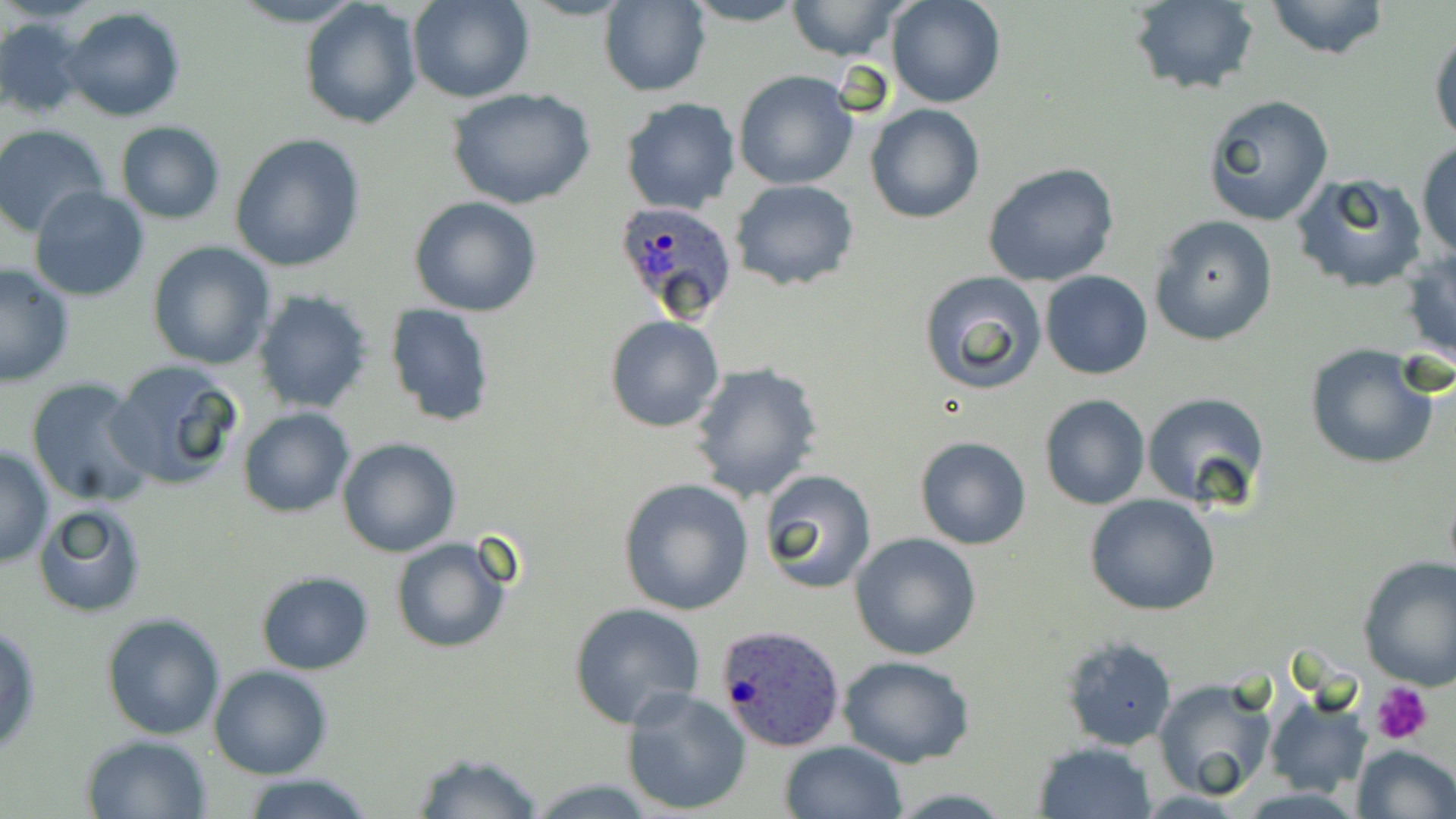
slide_level_diagnosis: Plasmodium ovale
field_of_view: one of a larger specimen
preparation: thin blood film
uninfected_red_blood_cell_locations: 'approximate bounding boxes as named x1/y1/x2/y2 corners in pixels: (x1=408, y1=0, x2=531, y2=104), (x1=599, y1=0, x2=710, y2=97), (x1=680, y1=0, x2=809, y2=27), (x1=786, y1=0, x2=909, y2=63), (x1=885, y1=0, x2=1005, y2=109), (x1=1262, y1=0, x2=1393, y2=60), (x1=298, y1=1, x2=421, y2=129), (x1=1126, y1=1, x2=1260, y2=95), (x1=61, y1=6, x2=188, y2=122), (x1=0, y1=18, x2=86, y2=118), (x1=1428, y1=20, x2=1456, y2=149), (x1=733, y1=71, x2=859, y2=190), (x1=450, y1=90, x2=595, y2=210), (x1=1204, y1=95, x2=1334, y2=225), (x1=620, y1=98, x2=742, y2=216), (x1=865, y1=102, x2=984, y2=223), (x1=115, y1=121, x2=226, y2=224), (x1=1, y1=126, x2=114, y2=239), (x1=229, y1=133, x2=367, y2=272), (x1=1416, y1=143, x2=1456, y2=262), (x1=981, y1=163, x2=1120, y2=287), (x1=1290, y1=173, x2=1429, y2=292), (x1=731, y1=180, x2=858, y2=290), (x1=30, y1=186, x2=151, y2=302), (x1=409, y1=196, x2=543, y2=317), (x1=1150, y1=216, x2=1278, y2=346), (x1=146, y1=242, x2=275, y2=370), (x1=1401, y1=251, x2=1456, y2=367), (x1=0, y1=261, x2=76, y2=387), (x1=917, y1=270, x2=1048, y2=394), (x1=1041, y1=271, x2=1152, y2=380), (x1=254, y1=289, x2=374, y2=415), (x1=386, y1=303, x2=496, y2=427), (x1=605, y1=315, x2=725, y2=434), (x1=1304, y1=346, x2=1440, y2=469), (x1=107, y1=360, x2=244, y2=492), (x1=689, y1=361, x2=823, y2=504), (x1=25, y1=378, x2=156, y2=508), (x1=1141, y1=391, x2=1272, y2=513), (x1=1040, y1=394, x2=1150, y2=510), (x1=238, y1=408, x2=355, y2=516), (x1=914, y1=436, x2=1033, y2=551), (x1=336, y1=437, x2=460, y2=557), (x1=0, y1=445, x2=54, y2=568), (x1=757, y1=470, x2=877, y2=592), (x1=617, y1=477, x2=755, y2=616), (x1=1084, y1=492, x2=1221, y2=615), (x1=34, y1=503, x2=147, y2=617), (x1=849, y1=532, x2=982, y2=661), (x1=390, y1=536, x2=514, y2=654), (x1=1356, y1=555, x2=1456, y2=691), (x1=254, y1=570, x2=375, y2=675), (x1=568, y1=601, x2=706, y2=728), (x1=101, y1=612, x2=227, y2=741), (x1=0, y1=624, x2=41, y2=758), (x1=1057, y1=634, x2=1176, y2=753), (x1=838, y1=655, x2=975, y2=769), (x1=209, y1=665, x2=331, y2=779), (x1=1153, y1=678, x2=1278, y2=801), (x1=621, y1=687, x2=751, y2=816), (x1=1263, y1=691, x2=1374, y2=797), (x1=79, y1=734, x2=212, y2=819), (x1=777, y1=740, x2=908, y2=819), (x1=1030, y1=740, x2=1158, y2=819), (x1=1351, y1=743, x2=1456, y2=819), (x1=408, y1=750, x2=545, y2=819), (x1=237, y1=772, x2=380, y2=819)'
stain: May-Grünwald-Giemsa
modality: light microscopy
magnification: 1000x
platelet_locations: 'approximate bounding boxes as named x1/y1/x2/y2 corners in pixels: (x1=1372, y1=680, x2=1435, y2=747)'
plasmodium_ovale_infected_red_blood_cell_locations: 'approximate bounding boxes as named x1/y1/x2/y2 corners in pixels: (x1=613, y1=198, x2=740, y2=321), (x1=716, y1=623, x2=847, y2=753)'
image_size: 1456×819 pixels